Identify the parasite.
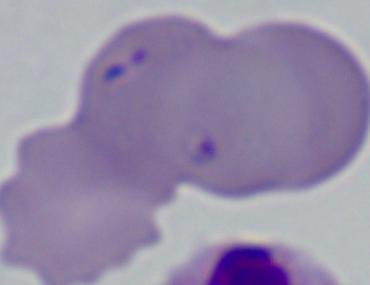

Babesia.

modality = micrograph
magnification = 1000x